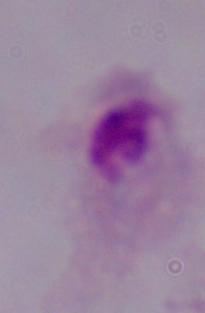 A trichomonad is shown. Micrograph. Captured at 1000x magnification.